Report the malaria status of this cell.
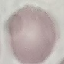

Uninfected.

Summary:
  - Preparation: thin blood film
  - Stain: Giemsa
  - Image type: cell patch, automatically extracted from a larger field of view and resized to 64 × 64 pixels
  - Capture: smartphone through the microscope eyepiece